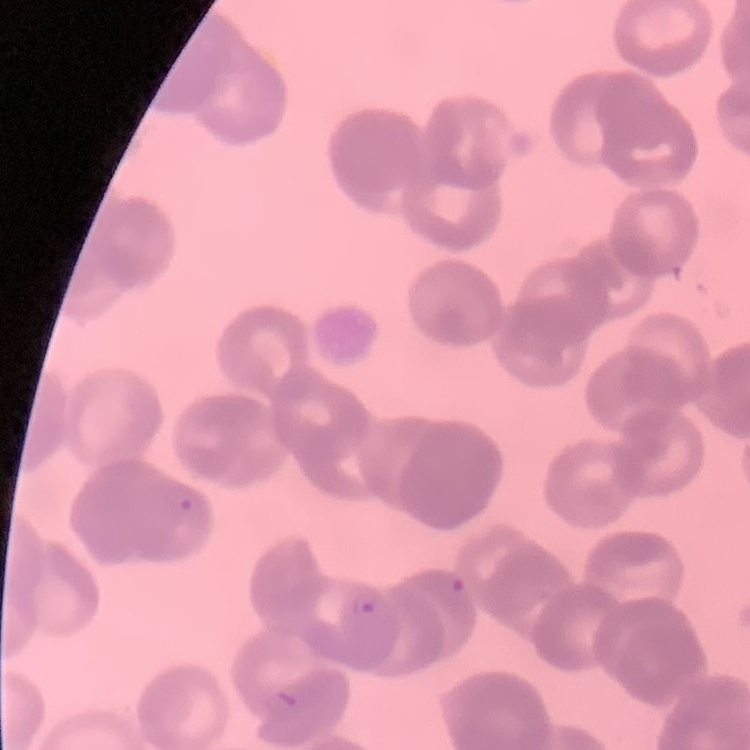
erythrocyte_morphology: rouleaux formation
image_type: one tile cut from a larger photomicrograph
stain: Field's or Giemsa
preparation: thin peripheral smear